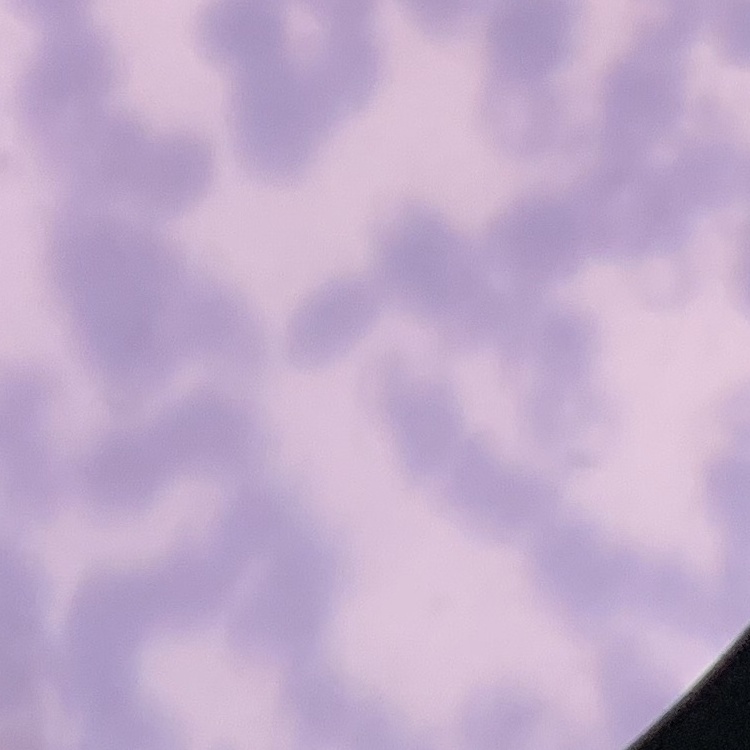

The red blood cells exhibit rouleaux formation. Square crop of a larger photomicrograph. Thin peripheral smear. Stained with either Field's or Giemsa.